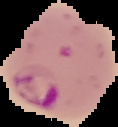

malaria status = parasitized
preparation = thin blood smear
image type = segmented cell region with the area outside set to black
image size = 118×127 pixels